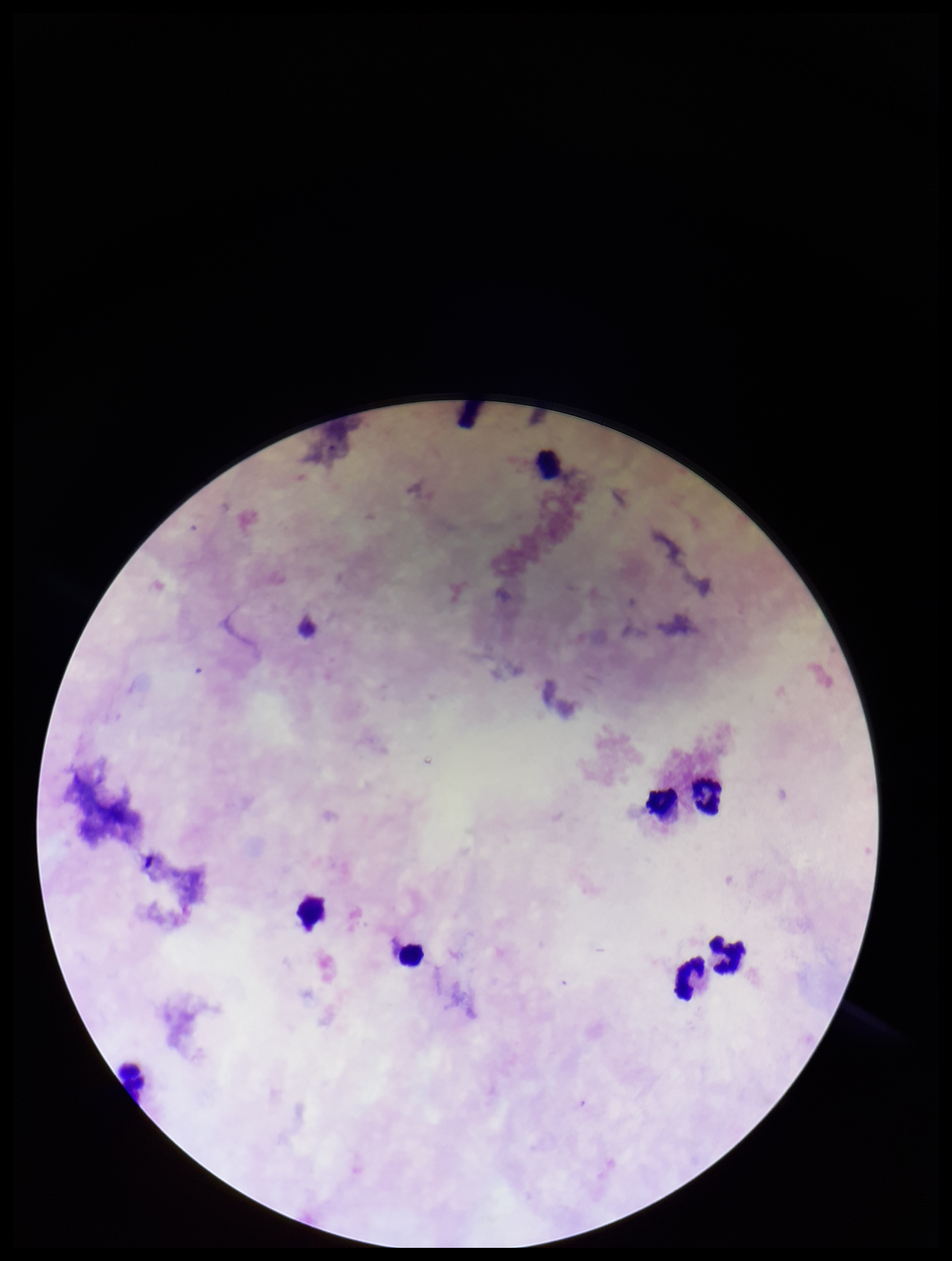

Summary:
  - Capture: smartphone photograph through the microscope eyepiece
  - Preparation: thick
  - Parasite count: 0
  - Leukocyte count: 8
  - Plasmodium parasites: none detected
  - Patient malaria status: negative
  - Stain: Giemsa
  - Field of view: one from this slide
  - Image size: 952×1261 pixels